Name the blood parasite species.
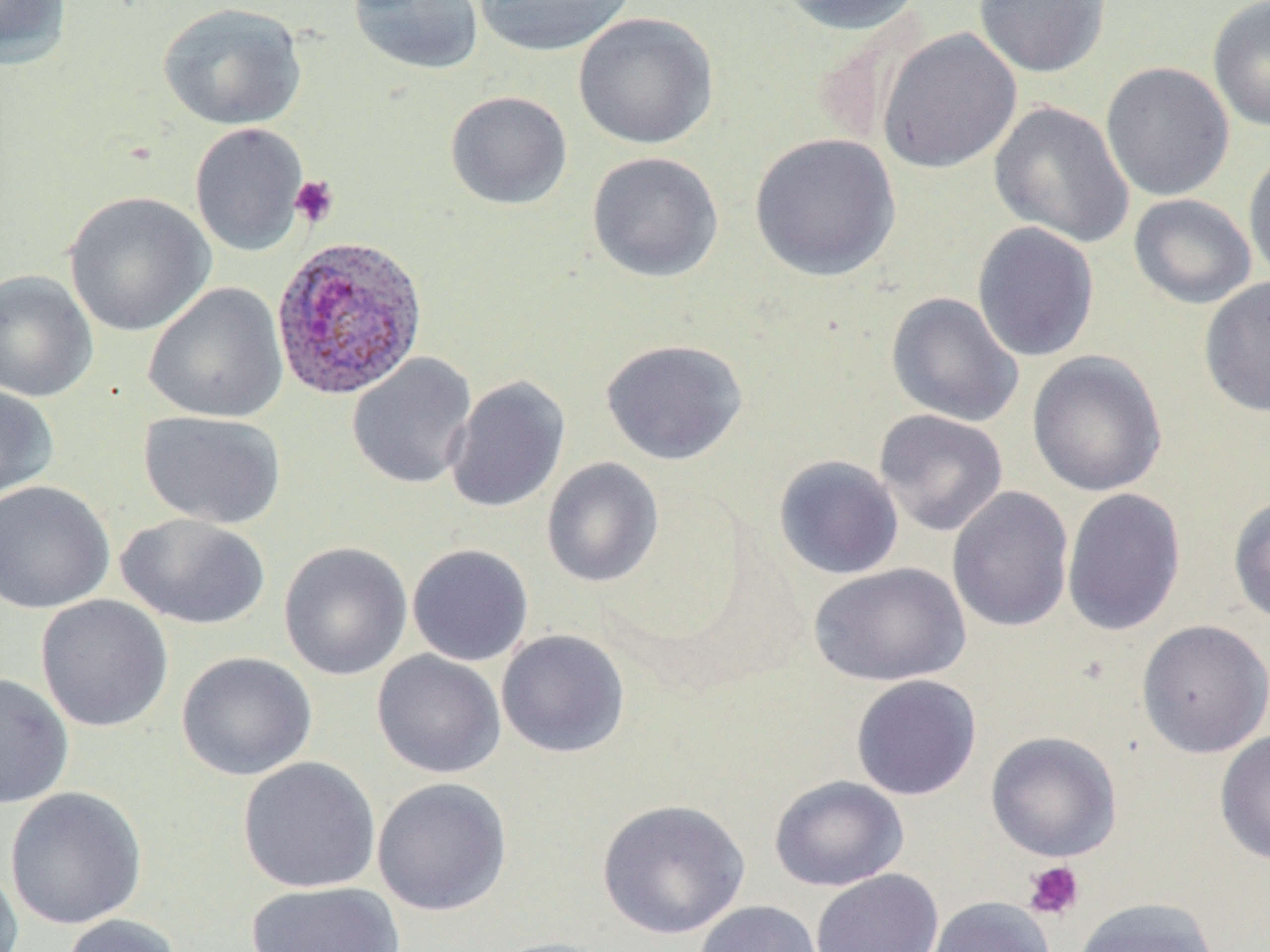
Plasmodium ovale.

Summary:
  - Coordinate format: approximate bounding boxes as named x1/y1/x2/y2 corners in pixels
  - Plasmodium ovale-infected red blood cell locations: (x1=270, y1=234, x2=428, y2=401)
  - Uninfected red blood cell locations: (x1=0, y1=0, x2=72, y2=71), (x1=348, y1=0, x2=484, y2=75), (x1=473, y1=0, x2=637, y2=57), (x1=772, y1=0, x2=927, y2=35), (x1=973, y1=0, x2=1111, y2=78), (x1=1207, y1=0, x2=1270, y2=133), (x1=157, y1=2, x2=307, y2=130), (x1=573, y1=12, x2=719, y2=150), (x1=877, y1=27, x2=1022, y2=174), (x1=1100, y1=61, x2=1235, y2=201), (x1=445, y1=90, x2=573, y2=210), (x1=989, y1=100, x2=1134, y2=248), (x1=189, y1=122, x2=309, y2=256), (x1=749, y1=133, x2=901, y2=282), (x1=1243, y1=147, x2=1270, y2=286), (x1=586, y1=151, x2=724, y2=283), (x1=64, y1=191, x2=215, y2=337), (x1=1128, y1=193, x2=1257, y2=310), (x1=971, y1=221, x2=1100, y2=362), (x1=0, y1=269, x2=99, y2=403), (x1=1198, y1=276, x2=1270, y2=418), (x1=143, y1=282, x2=289, y2=423), (x1=886, y1=292, x2=1024, y2=427), (x1=599, y1=338, x2=748, y2=466), (x1=1027, y1=350, x2=1168, y2=497), (x1=347, y1=352, x2=477, y2=489), (x1=444, y1=375, x2=570, y2=514), (x1=0, y1=385, x2=58, y2=501), (x1=874, y1=409, x2=1008, y2=537), (x1=139, y1=410, x2=287, y2=530), (x1=773, y1=454, x2=904, y2=581), (x1=541, y1=457, x2=664, y2=588), (x1=0, y1=480, x2=115, y2=614), (x1=947, y1=486, x2=1074, y2=632), (x1=1061, y1=488, x2=1186, y2=636), (x1=1227, y1=493, x2=1270, y2=626), (x1=116, y1=513, x2=270, y2=631), (x1=278, y1=541, x2=413, y2=681), (x1=407, y1=543, x2=534, y2=666), (x1=809, y1=562, x2=971, y2=687), (x1=35, y1=594, x2=173, y2=732), (x1=1136, y1=619, x2=1270, y2=758), (x1=496, y1=629, x2=631, y2=759), (x1=372, y1=650, x2=506, y2=779), (x1=176, y1=651, x2=317, y2=781), (x1=0, y1=672, x2=74, y2=809), (x1=850, y1=674, x2=982, y2=800), (x1=1214, y1=729, x2=1270, y2=866), (x1=985, y1=731, x2=1122, y2=862), (x1=237, y1=756, x2=381, y2=893), (x1=768, y1=775, x2=909, y2=892), (x1=372, y1=777, x2=512, y2=916), (x1=4, y1=786, x2=148, y2=931), (x1=596, y1=798, x2=751, y2=939), (x1=0, y1=859, x2=24, y2=952), (x1=810, y1=868, x2=943, y2=952), (x1=244, y1=880, x2=406, y2=952), (x1=926, y1=896, x2=1056, y2=952), (x1=1072, y1=897, x2=1220, y2=952), (x1=693, y1=900, x2=823, y2=952), (x1=58, y1=913, x2=184, y2=952), (x1=483, y1=937, x2=621, y2=952)
  - Platelet locations: (x1=290, y1=175, x2=340, y2=227), (x1=1023, y1=860, x2=1085, y2=920)
  - Stain: May-Grünwald-Giemsa
  - Modality: optical microscopy
  - Magnification: 1000x
  - Field of view: single
  - Preparation: thin blood smear
  - Image size: 1270×952 pixels